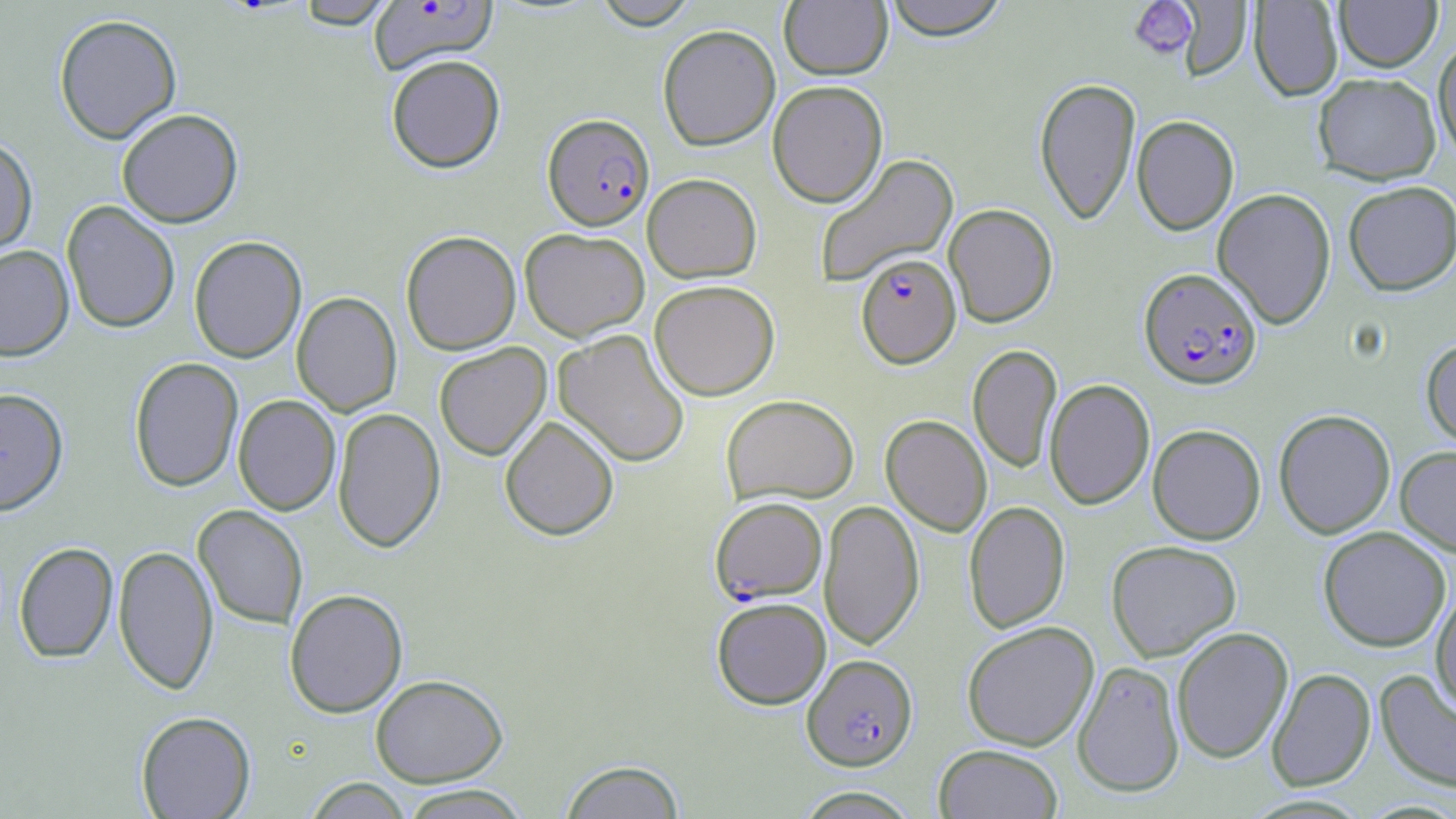

Summary:
  - Coordinate format: approximate bounding boxes as [x1, y1, x2, y2] in pixels
  - Plasmodium falciparum-infected red blood cell locations: [369, 1, 497, 74], [543, 114, 654, 231], [856, 253, 961, 368], [1139, 267, 1262, 389], [710, 497, 826, 603], [802, 654, 918, 770]
  - Uninfected red blood cell locations: [592, 0, 699, 29], [882, 0, 1010, 40], [1175, 0, 1253, 81], [1335, 0, 1442, 72], [292, 1, 398, 29], [779, 1, 893, 79], [1249, 1, 1343, 101], [53, 13, 182, 144], [657, 23, 780, 151], [1433, 38, 1456, 162], [386, 54, 505, 172], [1312, 72, 1442, 184], [1034, 77, 1141, 224], [768, 80, 888, 207], [116, 108, 243, 228], [1132, 115, 1239, 235], [0, 135, 38, 257], [814, 153, 959, 288], [642, 173, 762, 282], [1343, 181, 1456, 295], [1212, 188, 1336, 329], [61, 200, 180, 333], [943, 203, 1058, 327], [520, 228, 650, 341], [401, 230, 521, 355], [189, 235, 307, 363], [0, 245, 74, 361], [649, 279, 780, 401], [292, 291, 401, 416], [553, 329, 691, 467], [1421, 338, 1456, 450], [434, 342, 551, 460], [967, 345, 1062, 473], [129, 357, 243, 491], [1044, 378, 1155, 510], [0, 387, 69, 515], [722, 394, 859, 505], [233, 395, 340, 515], [333, 407, 445, 553], [1273, 409, 1396, 539], [499, 415, 619, 540], [881, 415, 992, 536], [1147, 424, 1266, 544], [1395, 445, 1456, 556], [819, 499, 924, 650], [964, 501, 1070, 633], [193, 505, 308, 629], [1318, 526, 1451, 652], [1106, 540, 1242, 662], [14, 542, 118, 663], [113, 544, 218, 695], [1431, 584, 1456, 714], [285, 589, 407, 717], [711, 597, 831, 709], [961, 621, 1099, 751], [1171, 626, 1293, 763], [1072, 660, 1185, 797], [1267, 667, 1376, 791], [1375, 669, 1456, 794], [371, 674, 507, 786], [136, 710, 255, 818], [933, 743, 1064, 819], [559, 759, 687, 818], [303, 778, 414, 818], [396, 785, 532, 818], [792, 786, 923, 818]
  - Platelet locations: [1129, 0, 1198, 59]
  - Slide-level diagnosis: Plasmodium falciparum
  - Image size: 1456×819 pixels
  - Modality: optical microscopy
  - Stain: May-Grünwald-Giemsa
  - Field of view: single
  - Preparation: thin blood smear
  - Magnification: 1000x